Identify the cell.
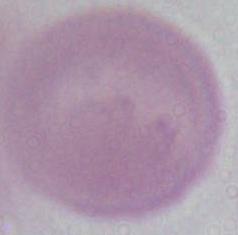
This is an erythrocyte.

Summary:
  - Magnification: 1000x
  - Modality: photomicrograph